State which parasite is depicted.
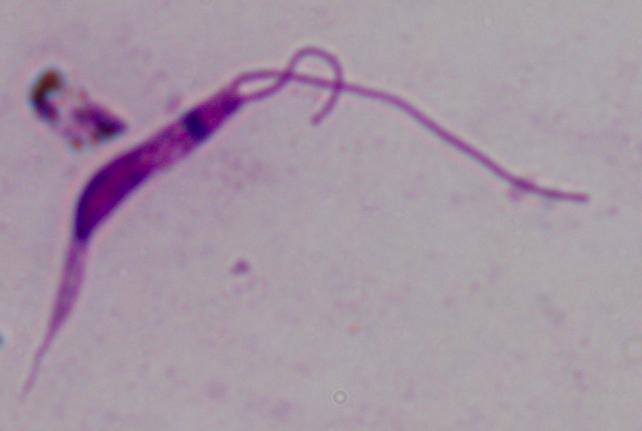
This is Leishmania.

magnification = 1000x
modality = photomicrograph